Locate every P. falciparum parasite and identify its life-cycle stage.
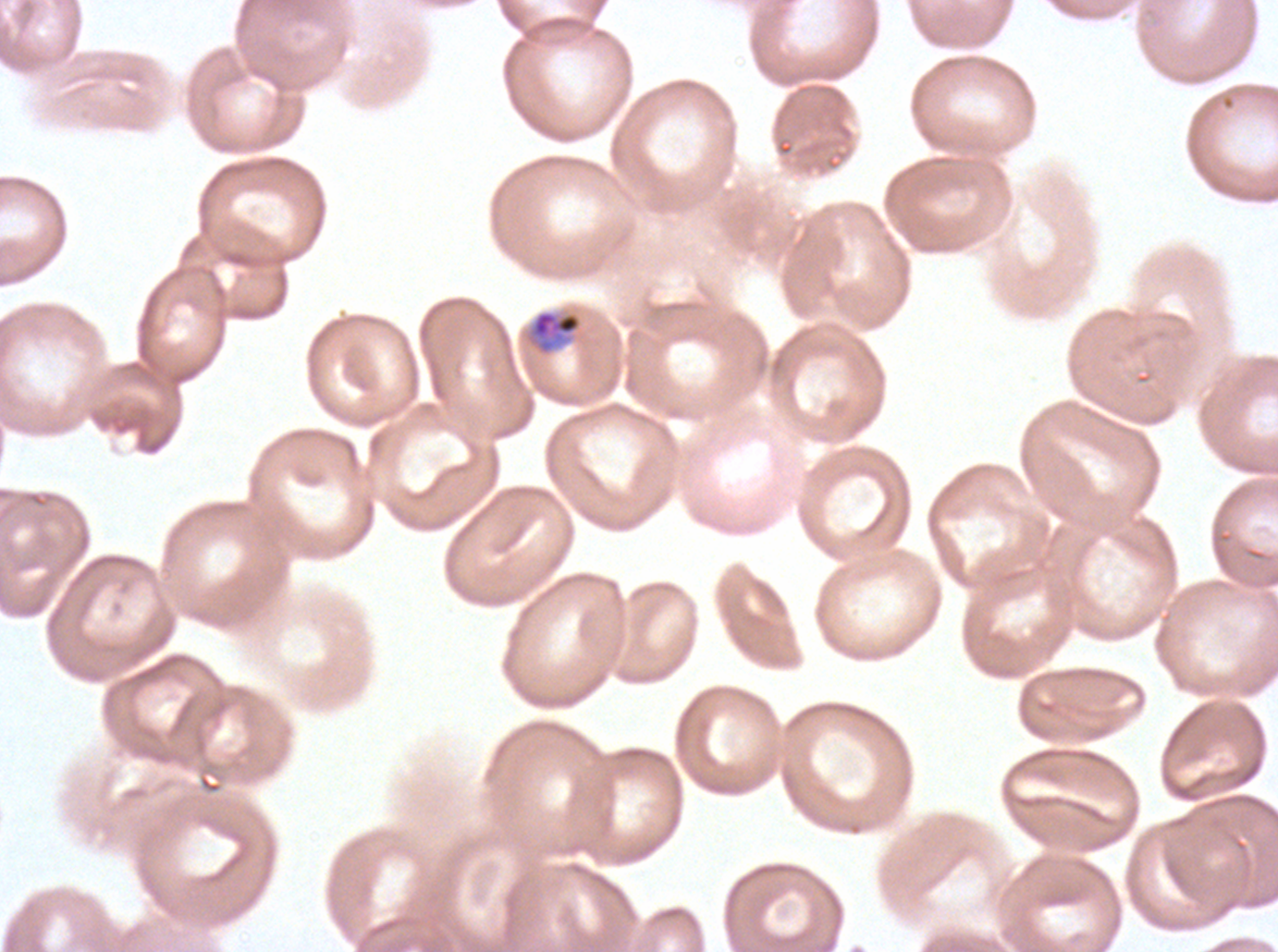

Approximate bounding boxes as (x1, y1, x2, y2) in pixels.
Late-ring/early-trophozoite forms: (528, 310, 583, 355).
No rings, mid trophozoites, late trophozoites, early schizonts, late schizonts, segmenters, or gametocytes observed.

Summary:
  - Field of view: one sub-image of a larger composite
  - Specimen: P. falciparum from a patient in The Gambia, cultured ex vivo for 24 to 48 hours
  - Preparation: thin blood film
  - Stain: Giemsa
  - Image size: 1278×952 pixels